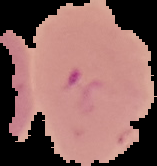

Summary:
  - Result: Plasmodium parasites detected
  - Image size: 157×166 pixels
  - Image type: segmented cell region with the area outside set to black
  - Preparation: thin blood film